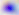
Summary:
  - Modality: photomicrograph
  - Magnification: 400x
  - Identification: Toxoplasma gondii